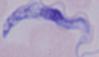

Captured at 1000x magnification. A trypanosome is seen. Photomicrograph.